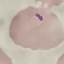
result = malaria parasites identified
capture = smartphone camera at the microscope eyepiece
image type = cell patch, automatically extracted from a larger field of view and resized to 64 × 64 pixels
stain = Giemsa
preparation = thin blood smear